Report the malaria status of this cell.
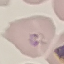

Parasitized.

preparation = thin blood film
stain = Giemsa
capture = smartphone through the microscope eyepiece
image type = automatically extracted cell patch, resized to 64 × 64 pixels